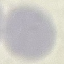

Summary:
  - Malaria status: uninfected
  - Stain: Giemsa
  - Image type: cell patch, automatically extracted from a larger field of view and resized to 64 × 64 pixels
  - Preparation: thin blood smear
  - Capture: smartphone camera at the microscope eyepiece